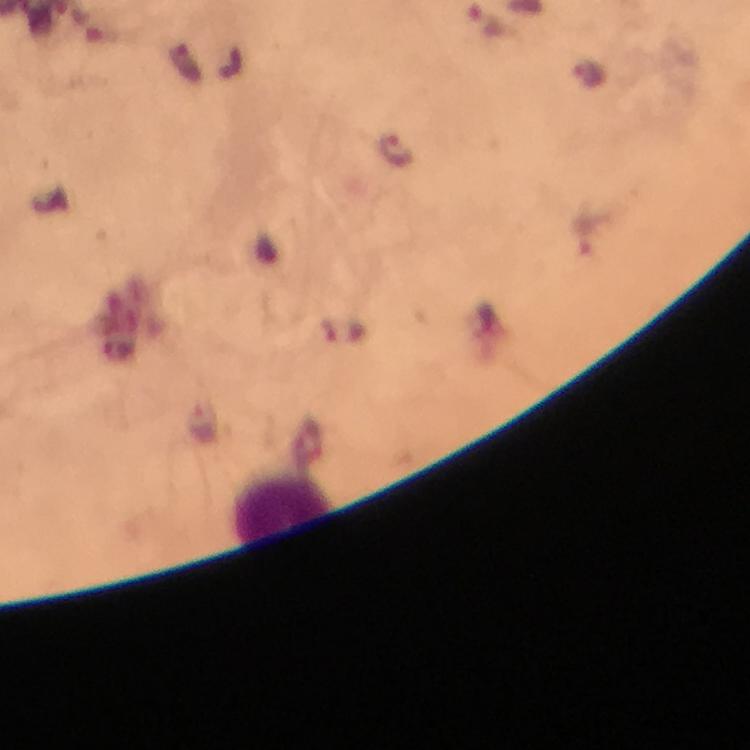

Approximate object centers, in pixels from the top-left corner.
Summary:
  - Malaria parasite locations: (x=488, y=23)
  - Leukocyte locations: (x=281, y=506)
  - Image size: 750×750 pixels
  - Context: from a diagnostic examination for malaria
  - Stain: Giemsa
  - Capture: smartphone photograph through a microscope
  - Cropped from: one field of view
  - Immersion oil: used
  - Preparation: thick smear
  - Magnification: 100x